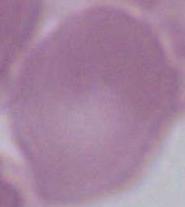
{
  "identification": "erythrocyte",
  "modality": "micrograph",
  "magnification": "1000x"
}